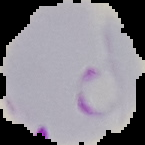
result = Plasmodium parasites detected
preparation = thin blood smear
image type = segmented cell region with the area outside set to black
image size = 145×145 pixels